Describe the morphology of the erythrocytes.
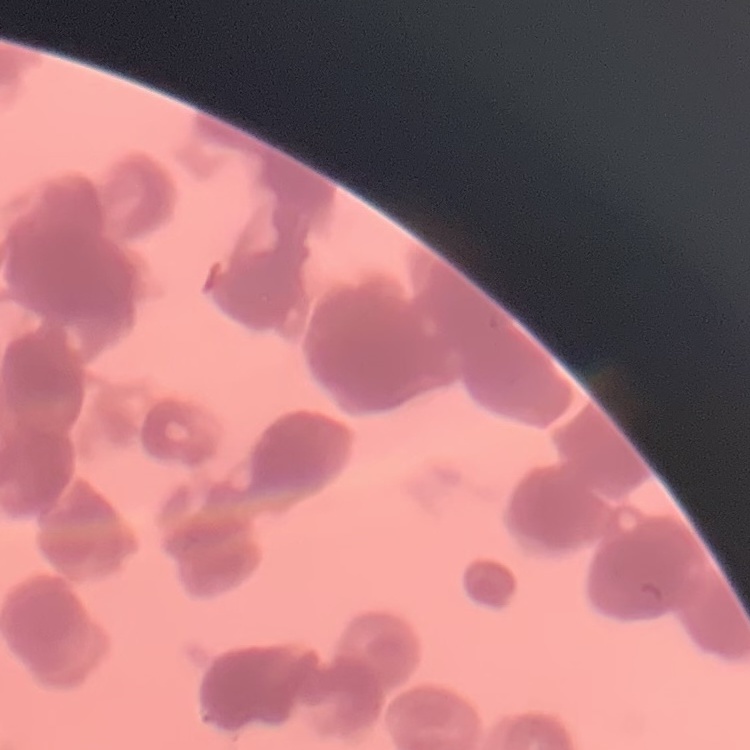

Rouleaux formation.

preparation = thin blood smear
stain = Field's or Giemsa
image type = square crop of a larger photomicrograph